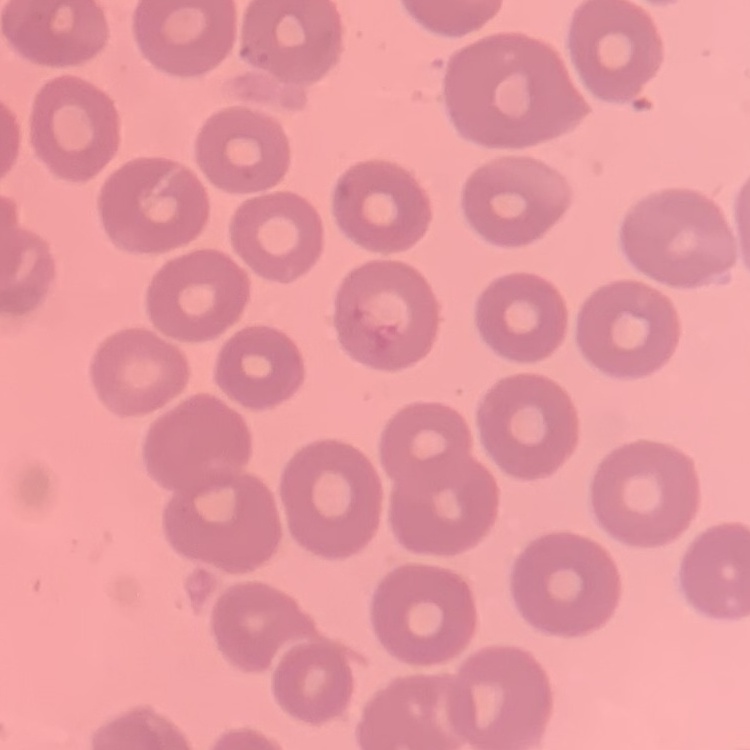

Summary:
  - Red blood cell morphology: no rouleaux formation
  - Preparation: thin blood film
  - Stain: Field's or Giemsa
  - Image type: square crop of a larger photomicrograph